Locate every Plasmodium falciparum parasite and give its life-cycle stage, and locate every leukocyte and any debris.
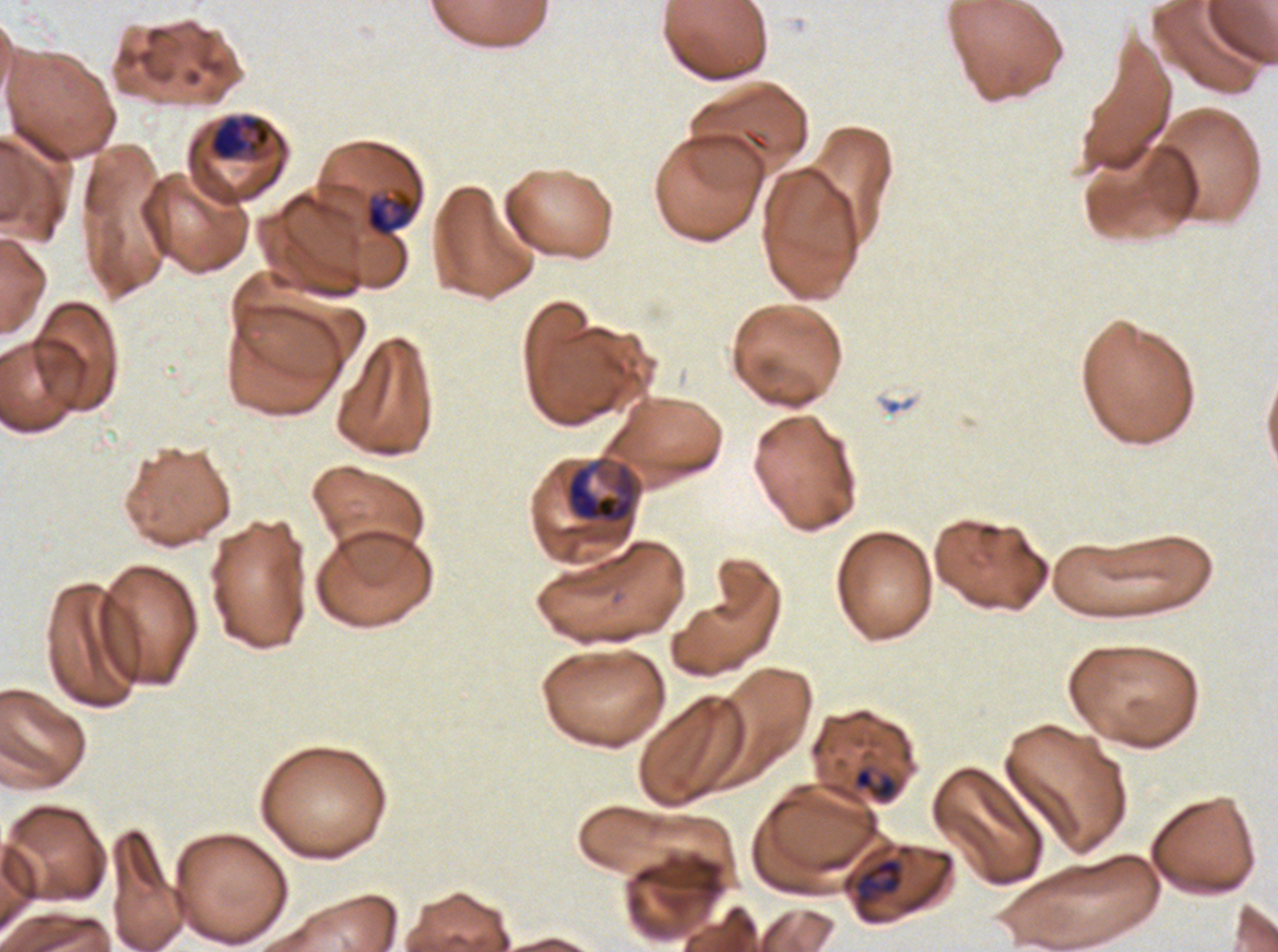

Approximate bounding boxes as [x1, y1, x2, y2] in pixels.
Late-ring/early-trophozoite forms: [853, 766, 898, 801].
Late trophozoites: [364, 190, 419, 238], [854, 857, 903, 905].
Early schizonts: [208, 114, 272, 162], [564, 454, 644, 539].
No rings, mid trophozoites, late schizonts, segmenters, gametocytes, leukocytes, or debris observed.

Image is 1278×952 pixels. Thin blood smear. Ex-vivo Plasmodium falciparum culture from a patient in The Gambia, grown for 24 to 48 hours. Life-cycle stages observed: late-ring/early-trophozoite, late trophozoite, early schizont. A sub-image separated from a larger composite. Giemsa-stained preparation.